Classify this cell by malaria status.
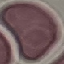

It is uninfected.

Acquired by smartphone through the microscope eyepiece. Thin blood film. Cell patch, automatically extracted from a larger field of view and resized to 64 × 64 pixels. Giemsa stain.